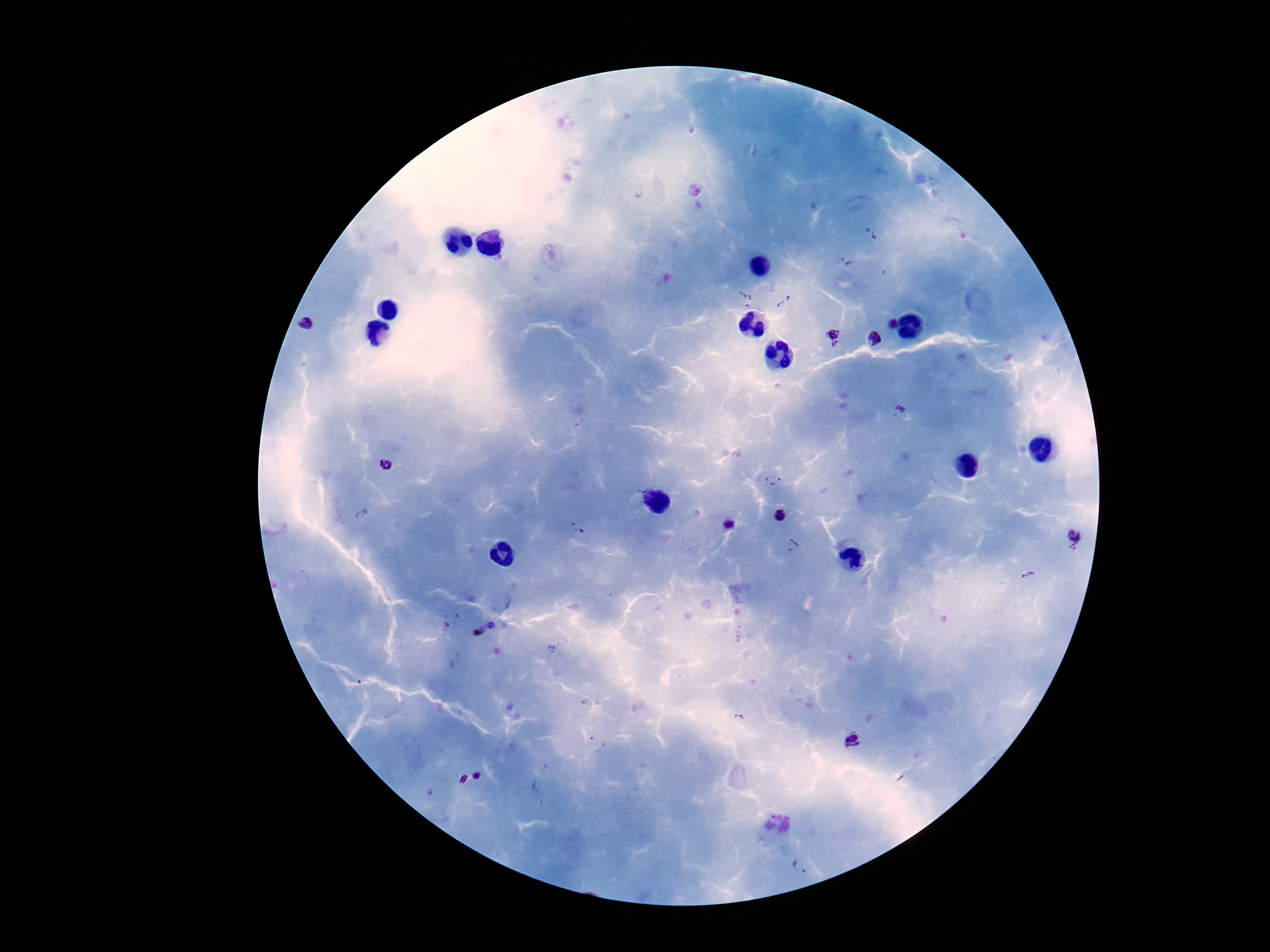

Approximate object centers, in pixels from the top-left corner. Plasmodium parasite locations: (x=871, y=233), (x=846, y=262), (x=745, y=298), (x=784, y=301), (x=891, y=324), (x=307, y=326), (x=833, y=334), (x=875, y=338), (x=836, y=348), (x=901, y=408), (x=386, y=465), (x=774, y=480), (x=780, y=514), (x=728, y=524), (x=578, y=528), (x=1073, y=535), (x=792, y=546), (x=1073, y=547), (x=1027, y=575), (x=447, y=625), (x=490, y=625), (x=478, y=632), (x=552, y=649), (x=852, y=742), (x=477, y=774), (x=461, y=779), (x=798, y=867). 100x magnification. Image is 1270×952 pixels. One field from this slide. Thick blood smear. Photographed through the microscope eyepiece with a smartphone camera. Patient malaria status: positive. Giemsa-stained preparation.